Identify the malaria species.
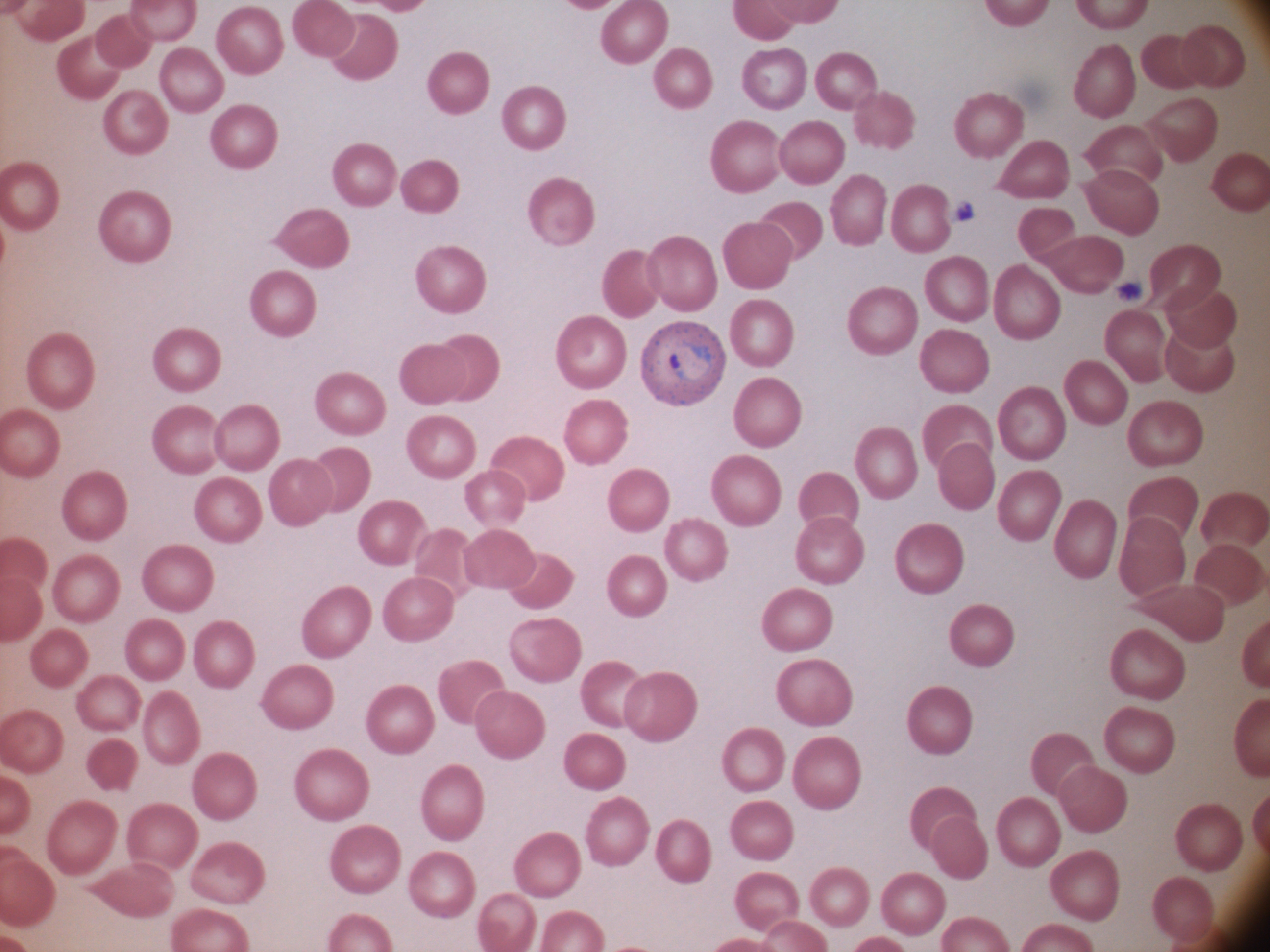
Plasmodium ovale.

Approximate bounding boxes as (x1,y1)-(x2,y2) corner pairs in pixels, from the source annotation, which is not necessarily exhaustive.
Summary:
  - Ring form locations: (666,345)-(713,382)
  - Image size: 1270×952 pixels
  - Preparation: thin blood smear
  - Field of view: one from this slide
  - Magnification: 100x
  - Microscope: Leica DM2000 with built-in camera
  - Stain: Giemsa